Classify this cell by malaria status.
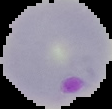

It is parasitized.

From a thin blood smear. The area outside the segmented cell region is set to black. Image is 112×109 pixels.